Classify this cell by malaria status.
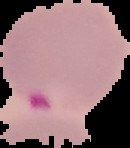
It is parasitized.

{
  "image_type": "cell region segmented out of the field of view; surrounding area masked to black",
  "image_size": "130×148 pixels",
  "preparation": "thin blood film"
}